Locate and identify every blood parasite.
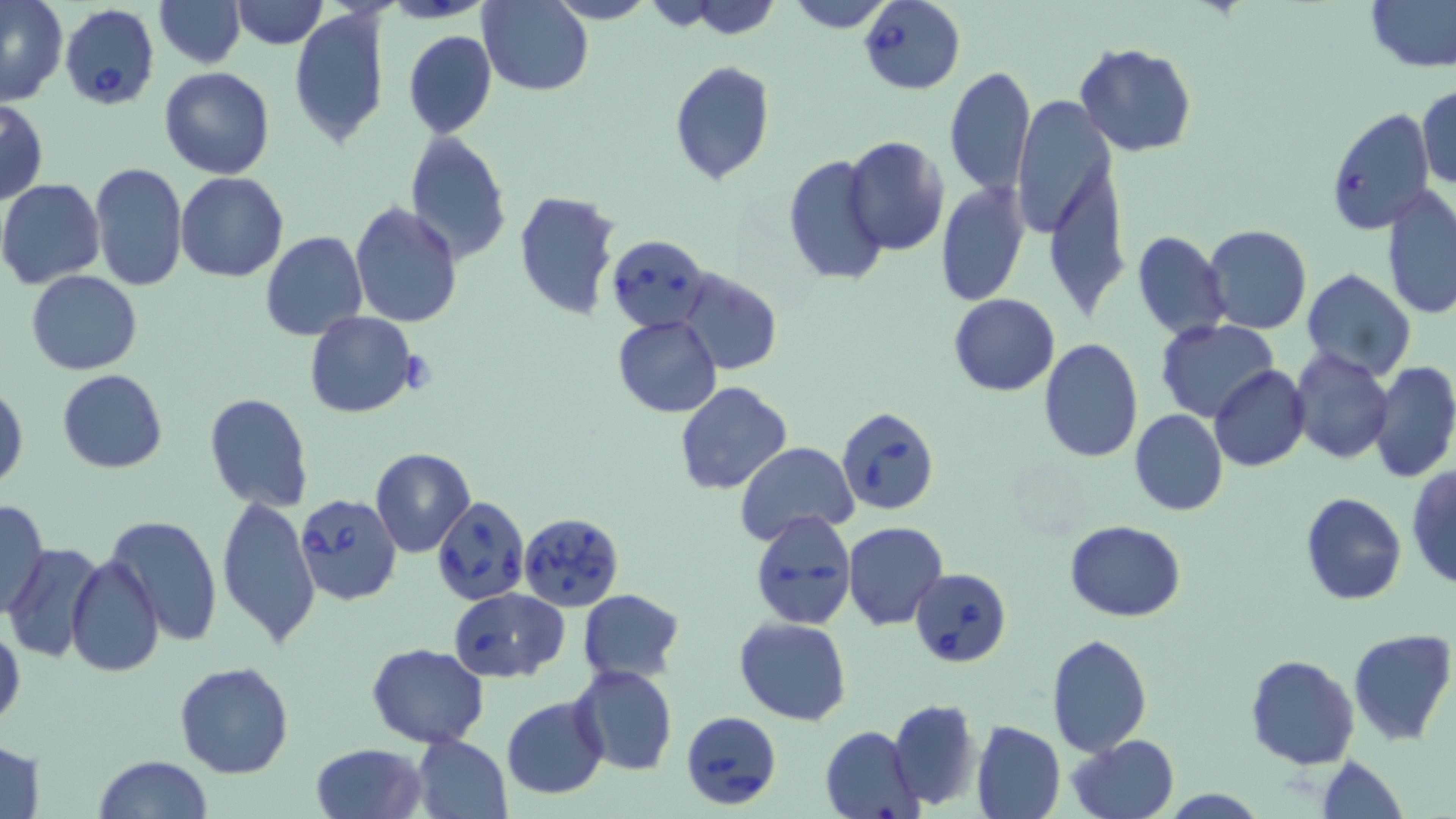

Approximate bounding boxes as [x1, y1, x2, y2] in pixels.
Babesia divergens-infected red blood cells: [859, 0, 966, 93], [55, 1, 159, 111], [1324, 109, 1436, 236], [606, 235, 710, 331], [837, 405, 941, 517], [296, 493, 403, 606], [433, 495, 530, 605], [749, 510, 856, 630], [517, 512, 624, 611], [911, 567, 1013, 667], [447, 587, 569, 682], [681, 710, 782, 810].
No Plasmodium falciparum, Plasmodium ovale, Plasmodium malariae, Plasmodium vivax, or Trypanosoma brucei observed.

Summary:
  - Uninfected red blood cell locations: [153, 0, 246, 67], [229, 0, 327, 47], [546, 0, 655, 24], [659, 0, 785, 37], [785, 0, 894, 32], [1363, 0, 1456, 73], [0, 2, 68, 106], [480, 2, 593, 96], [289, 7, 388, 150], [404, 30, 497, 138], [1073, 43, 1199, 157], [669, 61, 775, 185], [158, 66, 275, 179], [945, 67, 1035, 196], [1416, 83, 1455, 190], [1011, 96, 1115, 238], [0, 97, 49, 206], [404, 130, 512, 264], [843, 137, 949, 256], [1040, 146, 1130, 325], [783, 153, 890, 290], [89, 162, 187, 293], [175, 172, 287, 282], [0, 179, 107, 289], [935, 181, 1029, 307], [1382, 186, 1456, 321], [514, 189, 624, 323], [350, 203, 462, 328], [1203, 224, 1312, 335], [1132, 230, 1230, 340], [260, 232, 367, 341], [1302, 268, 1415, 379], [675, 269, 781, 376], [27, 271, 142, 375], [948, 294, 1059, 396], [304, 312, 420, 418], [612, 314, 722, 418], [1156, 319, 1278, 421], [1039, 337, 1143, 463], [1288, 349, 1393, 464], [1368, 360, 1456, 484], [1210, 366, 1310, 471], [57, 369, 167, 473], [0, 379, 27, 493], [676, 381, 791, 496], [205, 393, 314, 511], [1130, 410, 1227, 517], [735, 441, 860, 542], [369, 447, 476, 558], [1406, 465, 1456, 590], [1301, 492, 1407, 605], [215, 493, 320, 648], [0, 498, 49, 619], [104, 514, 221, 649], [842, 521, 948, 630], [1064, 521, 1187, 621], [5, 543, 109, 664], [65, 553, 164, 677], [577, 588, 685, 683], [734, 616, 852, 725], [0, 621, 25, 736], [1348, 630, 1456, 746], [1048, 634, 1152, 755], [367, 643, 489, 747], [1245, 653, 1359, 769], [175, 661, 295, 779], [570, 664, 677, 777], [501, 695, 609, 801], [888, 697, 980, 810], [970, 719, 1065, 819], [821, 725, 924, 818], [411, 735, 511, 819], [1067, 736, 1179, 819], [0, 738, 46, 818], [310, 742, 428, 819], [1316, 754, 1408, 819], [94, 755, 214, 819], [1164, 787, 1267, 818]
  - Slide-level diagnosis: Babesia divergens
  - Image size: 1456×819 pixels
  - Preparation: thin blood smear
  - Magnification: 1000x
  - Modality: light microscopy
  - Field of view: single
  - Stain: May-Grünwald-Giemsa